Locate every blood parasite and identify its species.
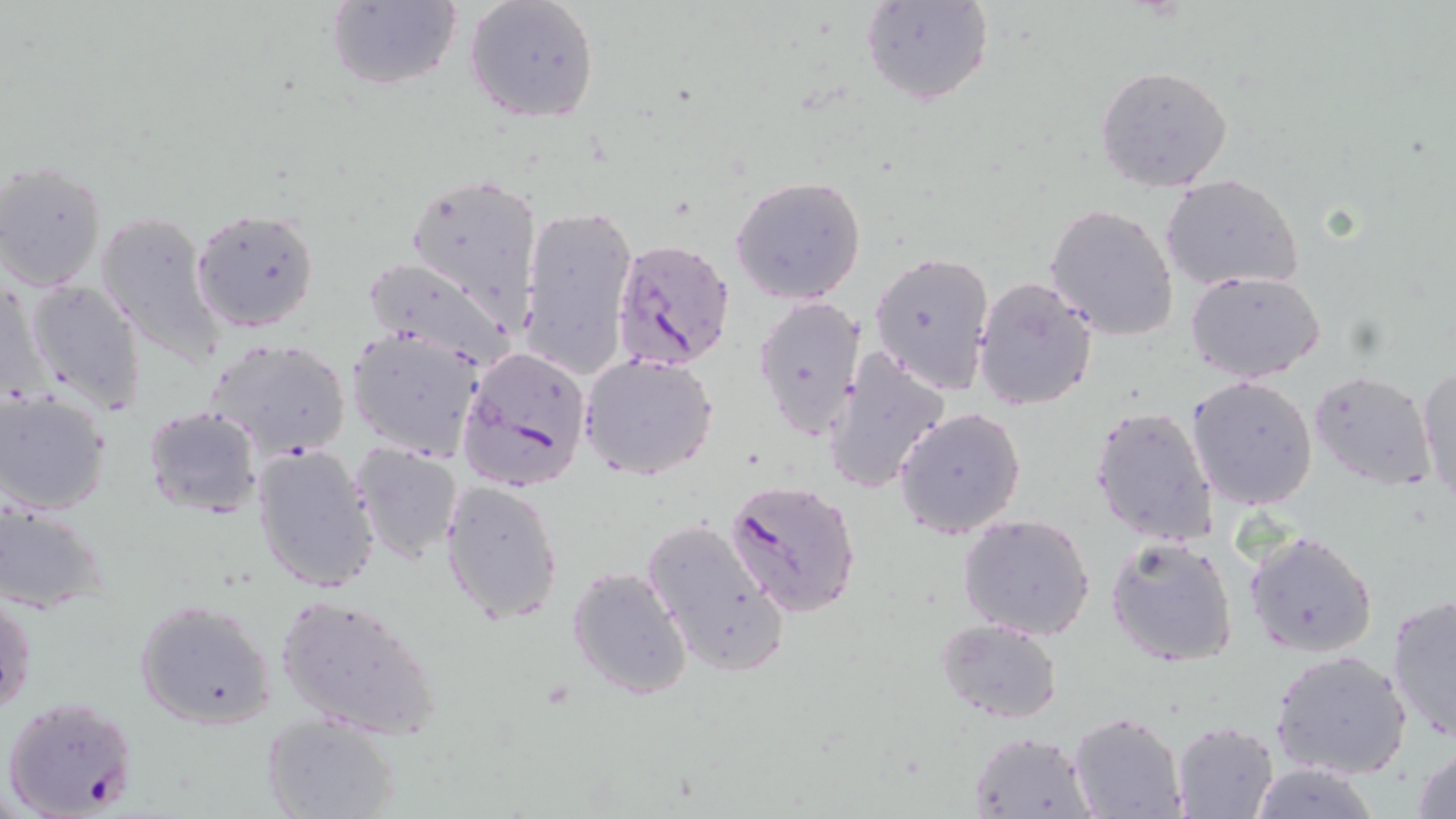
Approximate bounding boxes as (x1, y1, x2, y2) in pixels.
Plasmodium falciparum-infected red blood cells: (611, 237, 735, 372), (458, 345, 593, 493), (725, 478, 861, 616), (2, 695, 139, 818).
No Plasmodium ovale, Plasmodium malariae, Plasmodium vivax, Babesia divergens, or Trypanosoma brucei observed.

{
  "slide_level_diagnosis": "Plasmodium falciparum",
  "modality": "light microscopy",
  "preparation": "thin blood film",
  "stain": "May-Grünwald-Giemsa",
  "image_size": "1456×819 pixels",
  "magnification": "1000x",
  "field_of_view": "single",
  "uninfected_red_blood_cell_locations": "approximate bounding boxes as (x1, y1, x2, y2) in pixels: (325, 0, 463, 92), (464, 0, 600, 125), (862, 0, 994, 107), (1095, 64, 1235, 195), (1, 161, 107, 291), (405, 169, 545, 329), (1160, 173, 1305, 293), (730, 175, 867, 306), (1046, 203, 1180, 342), (518, 204, 638, 381), (191, 207, 322, 333), (96, 211, 229, 368), (869, 250, 995, 395), (360, 256, 514, 366), (1186, 270, 1326, 383), (973, 276, 1099, 413), (24, 278, 147, 413), (1, 283, 47, 404), (752, 295, 867, 442), (346, 328, 485, 459), (204, 337, 352, 461), (823, 349, 952, 494), (580, 354, 719, 481), (1417, 362, 1455, 505), (1308, 370, 1436, 491), (1185, 374, 1318, 509), (0, 391, 113, 515), (1089, 404, 1218, 547), (143, 405, 264, 518), (894, 406, 1026, 540), (250, 443, 382, 595), (350, 445, 463, 565), (440, 479, 564, 624), (0, 501, 109, 613), (957, 514, 1097, 642), (641, 517, 788, 677), (1244, 530, 1378, 657), (1106, 536, 1238, 668), (567, 565, 693, 699), (0, 588, 38, 720), (274, 592, 442, 740), (1386, 594, 1455, 744), (134, 598, 278, 730), (936, 617, 1062, 725), (1271, 648, 1411, 780), (1067, 712, 1187, 819), (260, 713, 401, 819), (1169, 720, 1281, 819), (969, 730, 1094, 817), (1412, 744, 1456, 819)"
}